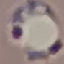
result = malaria parasites detected
capture = smartphone camera at the microscope eyepiece
stain = Giemsa
preparation = thin blood film
image type = automatically extracted cell patch, resized to 64 × 64 pixels